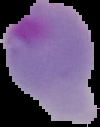

Summary:
  - Image size: 100×127 pixels
  - Preparation: thin blood smear
  - Malaria status: parasitized
  - Image type: segmented cell region on a black background